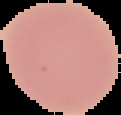

image size = 121×115 pixels
malaria status = uninfected
image type = cell region segmented out of the field of view; surrounding area masked to black
preparation = thin blood smear